Identify the cell.
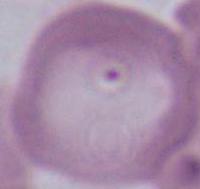
This is an erythrocyte.

Photomicrograph. Captured at 1000x magnification.